Name the parasite shown.
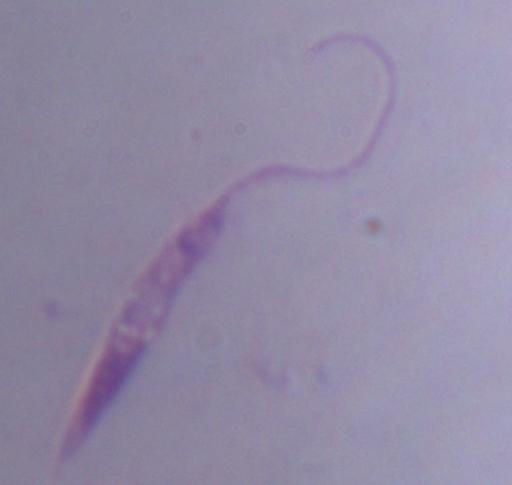

This is Leishmania.

Summary:
  - Modality: micrograph
  - Magnification: 1000x